Assess the morphology of the red blood cells.
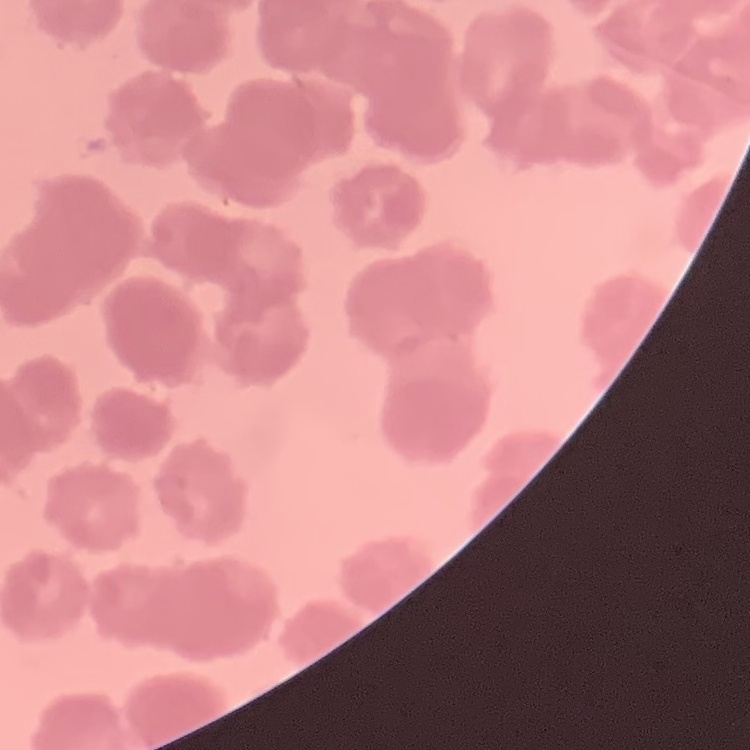

They show rouleaux formation.

Field's or Giemsa stain. Square crop of a larger photomicrograph. Thin blood film.